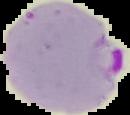
image type = segmented cell region with the area outside set to black
preparation = thin blood film
image size = 130×115 pixels
result = malaria parasites identified